Assess this cell for malaria.
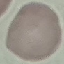
Uninfected.

Summary:
  - Image type: cell patch, automatically extracted from a larger field of view and resized to 64 × 64 pixels
  - Capture: smartphone camera at the microscope eyepiece
  - Preparation: thin blood film
  - Stain: Giemsa